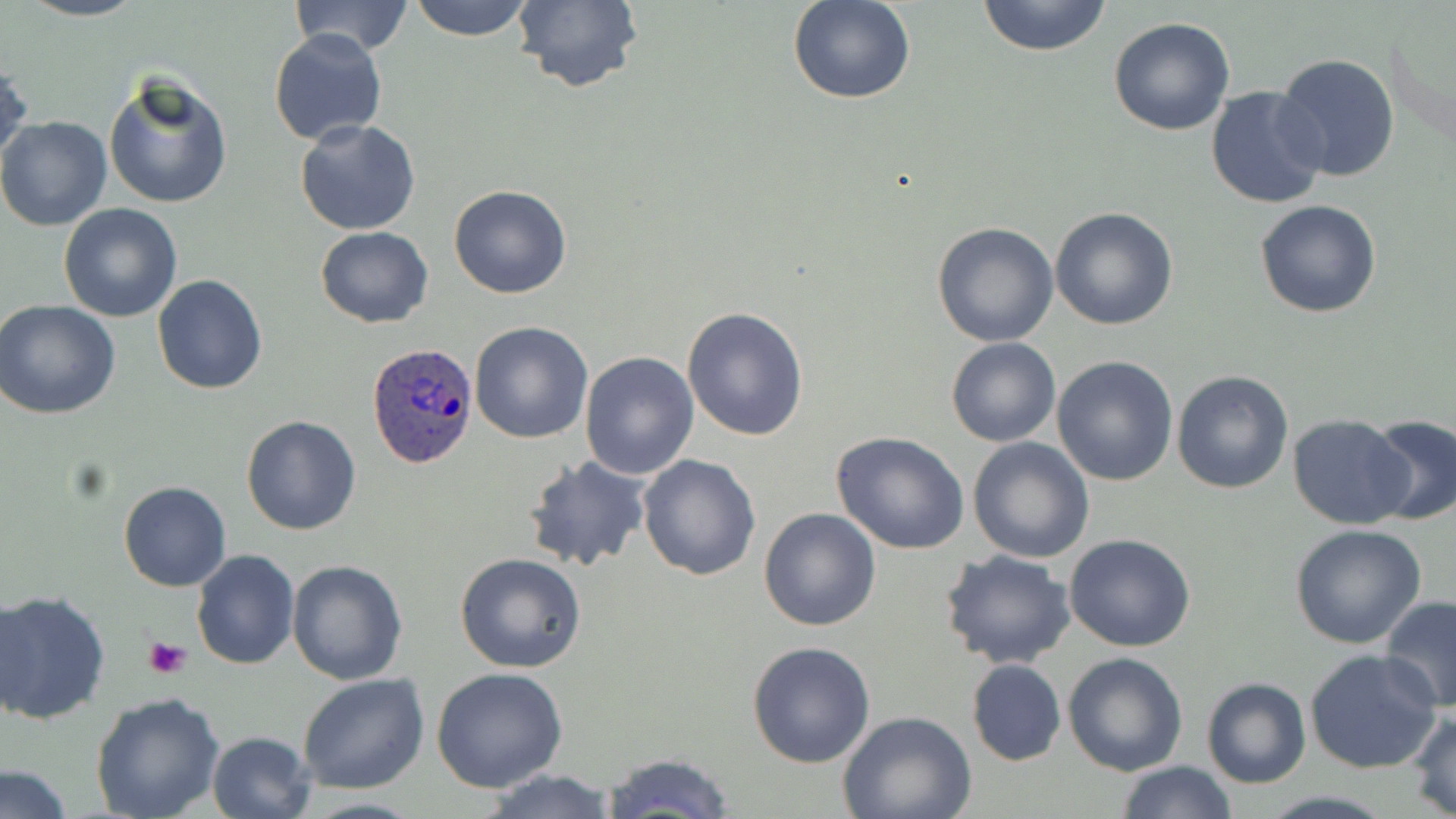
{
  "plasmodium_ovale_infected_red_blood_cell_locations": "approximate bounding boxes as (x1,y1)-(x2,y2) corner pairs in pixels: (367,341)-(478,469)",
  "slide_level_diagnosis": "Plasmodium ovale",
  "image_size": "1456×819 pixels",
  "uninfected_red_blood_cell_locations": "approximate bounding boxes as (x1,y1)-(x2,y2) corner pairs in pixels: (18,0)-(148,22), (289,0)-(416,58), (407,0)-(535,40), (510,0)-(643,95), (977,0)-(1112,57), (789,1)-(914,104), (1108,17)-(1235,136), (269,29)-(389,146), (1273,53)-(1400,182), (0,55)-(29,173), (103,74)-(233,210), (1205,85)-(1330,211), (0,116)-(112,232), (295,120)-(422,236), (448,185)-(573,298), (1255,199)-(1382,319), (58,203)-(183,322), (1050,207)-(1179,331), (932,222)-(1059,346), (315,227)-(434,327), (152,274)-(268,394), (0,301)-(121,419), (682,307)-(808,440), (470,320)-(595,443), (946,337)-(1060,448), (580,350)-(701,479), (1052,355)-(1180,486), (1172,371)-(1295,494), (1288,414)-(1412,530), (1363,414)-(1455,525), (241,415)-(361,535), (831,432)-(970,554), (967,437)-(1093,562), (522,454)-(651,574), (638,454)-(762,579), (118,480)-(231,592), (758,507)-(883,631), (1289,524)-(1427,648), (1062,532)-(1196,652), (191,549)-(300,671), (939,549)-(1076,669), (455,553)-(587,674), (287,560)-(410,685), (0,590)-(112,725), (1378,595)-(1456,714), (747,641)-(876,768), (1306,649)-(1441,776), (1062,652)-(1187,776), (965,659)-(1066,767), (431,666)-(568,792), (297,673)-(428,794), (1200,677)-(1312,789), (91,691)-(225,819), (1409,707)-(1456,817), (838,711)-(976,819), (207,731)-(318,819), (598,752)-(737,818), (1116,760)-(1236,818), (2,766)-(72,818), (479,769)-(623,819)",
  "stain": "May-Grünwald-Giemsa",
  "preparation": "thin blood smear",
  "field_of_view": "one of a larger specimen",
  "modality": "light microscopy",
  "magnification": "1000x",
  "platelet_locations": "approximate bounding boxes as (x1,y1)-(x2,y2) corner pairs in pixels: (144,639)-(190,680)"
}